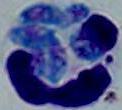
Photomicrograph. A white blood cell is shown. 1000x magnification.